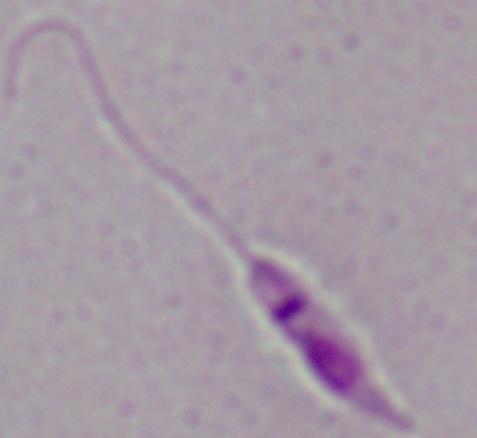

{
  "identification": "Leishmania",
  "modality": "micrograph",
  "magnification": "1000x"
}